Report the malaria status of this cell.
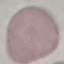

Uninfected.

Summary:
  - Stain: Giemsa
  - Preparation: thin blood film
  - Capture: smartphone through the microscope eyepiece
  - Image type: cell patch, automatically extracted from a larger field of view and resized to 64 × 64 pixels